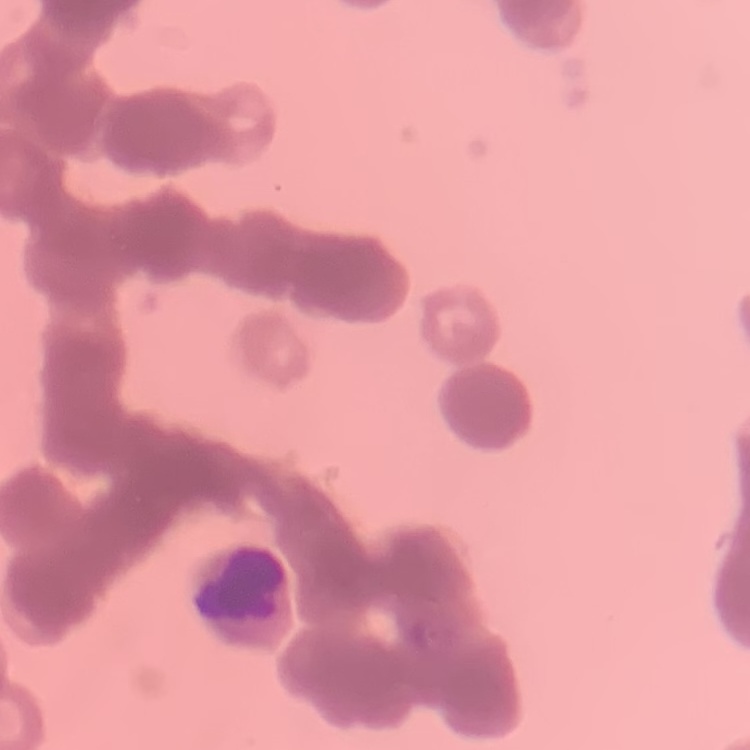
Summary:
  - Erythrocyte morphology: rouleaux formation
  - Stain: Field's or Giemsa
  - Image type: square crop of a larger photomicrograph
  - Preparation: thin blood film